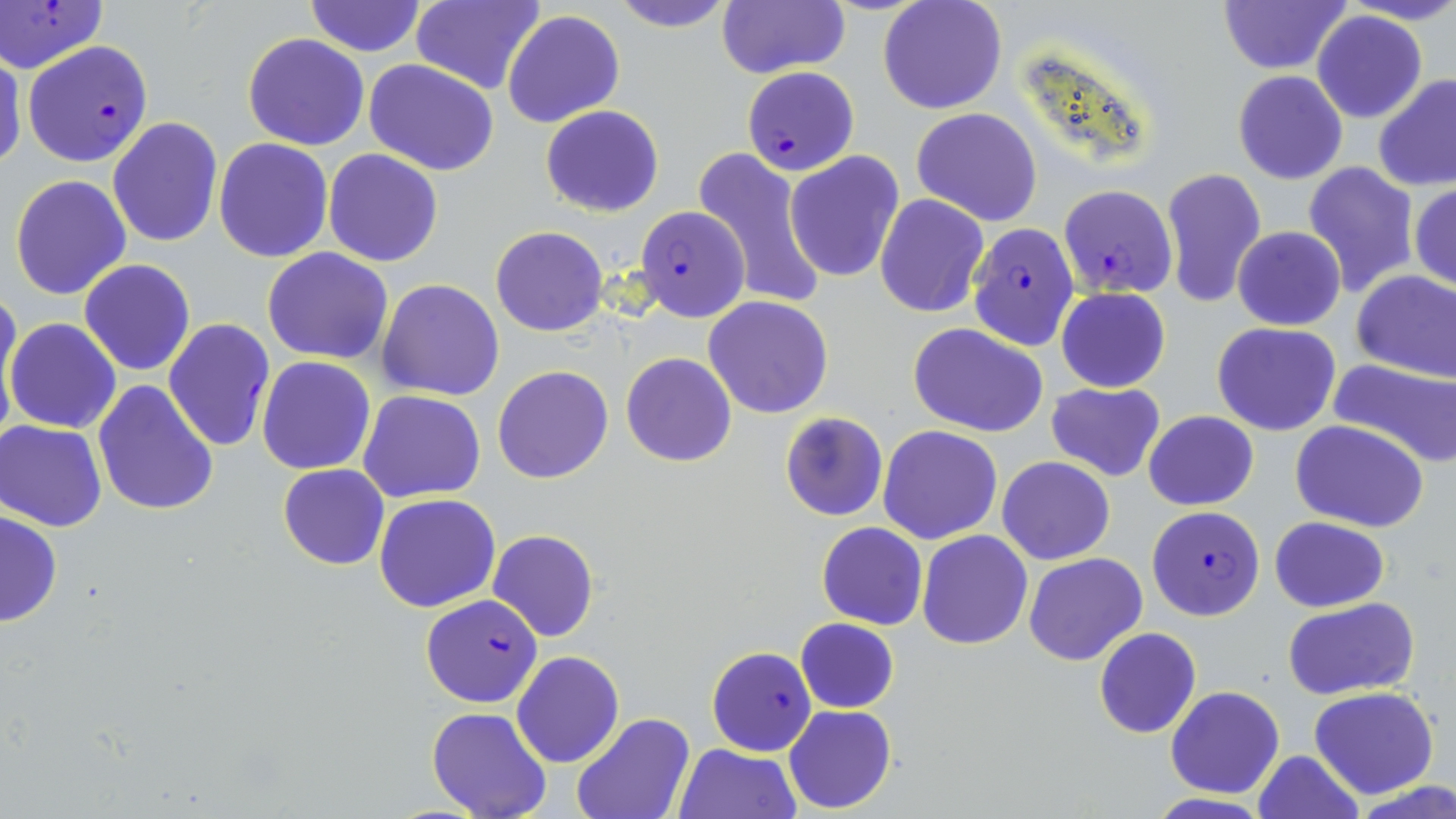
Plasmodium falciparum-infected red blood cell locations = approximate bounding boxes as [x1, y1, x2, y2] in pixels: [1, 0, 108, 74], [22, 40, 153, 166], [741, 66, 859, 176], [1057, 183, 1177, 296], [636, 207, 748, 322], [968, 221, 1080, 352], [164, 317, 275, 452], [1146, 505, 1265, 621], [419, 594, 543, 708], [706, 646, 817, 755]
slide-level diagnosis = Plasmodium falciparum
image size = 1456×819 pixels
uninfected red blood cell locations = approximate bounding boxes as [x1, y1, x2, y2] in pixels: [410, 0, 544, 95], [609, 0, 737, 32], [718, 0, 848, 79], [878, 0, 1007, 115], [1218, 0, 1348, 74], [304, 2, 426, 56], [502, 8, 626, 129], [1312, 11, 1428, 123], [242, 32, 369, 150], [0, 50, 26, 171], [364, 58, 498, 175], [1231, 70, 1348, 184], [1374, 73, 1456, 191], [540, 104, 663, 217], [911, 107, 1042, 227], [108, 116, 224, 248], [213, 137, 335, 262], [692, 145, 827, 312], [323, 148, 443, 268], [785, 151, 905, 284], [1302, 161, 1420, 296], [1160, 167, 1267, 306], [9, 174, 131, 301], [1410, 182, 1455, 291], [875, 193, 989, 318], [491, 225, 608, 338], [1232, 227, 1346, 330], [263, 247, 395, 363], [79, 259, 196, 376], [1351, 269, 1456, 381], [377, 279, 506, 401], [1057, 287, 1170, 392], [0, 290, 22, 420], [702, 296, 833, 419], [6, 317, 122, 435], [1214, 321, 1341, 436], [909, 322, 1049, 437], [621, 352, 737, 467], [257, 356, 376, 475], [1327, 358, 1456, 468], [493, 365, 614, 483], [93, 380, 220, 519], [1047, 381, 1166, 481], [357, 389, 485, 503], [1143, 409, 1258, 511], [780, 412, 886, 522], [1, 420, 110, 530], [1291, 421, 1429, 532], [878, 425, 1003, 545], [997, 457, 1115, 566], [277, 464, 389, 569], [373, 492, 501, 613], [1, 510, 63, 628], [1270, 517, 1391, 612], [817, 522, 927, 630], [487, 530, 599, 642], [917, 530, 1033, 650], [1024, 552, 1147, 666], [1281, 597, 1419, 700], [795, 618, 898, 713], [1093, 626, 1202, 740], [512, 650, 625, 767], [1309, 685, 1439, 798], [1165, 686, 1284, 798], [784, 705, 896, 813], [427, 708, 552, 818], [571, 711, 695, 819], [673, 742, 801, 819], [1252, 750, 1365, 819], [1357, 783, 1456, 819], [1144, 793, 1278, 819]
stain = May-Grünwald-Giemsa
field of view = single
preparation = thin blood film
modality = optical microscopy
magnification = 1000x